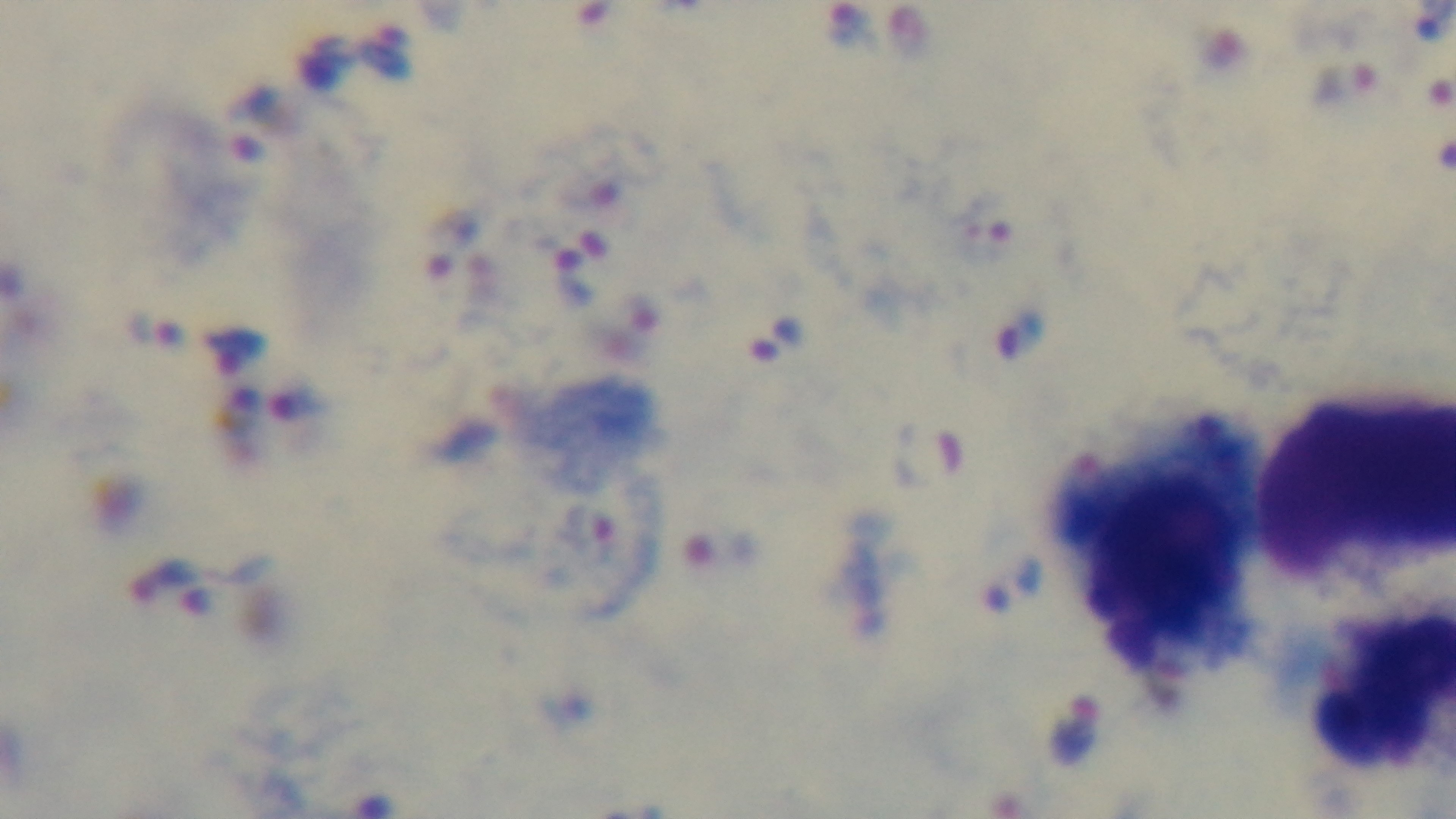

Giemsa-stained. Preparation: thick. 100x oil-immersion objective. Light microscopy. Malaria status: infected. Single field of view. Captured with a mounted 4K digital camera.